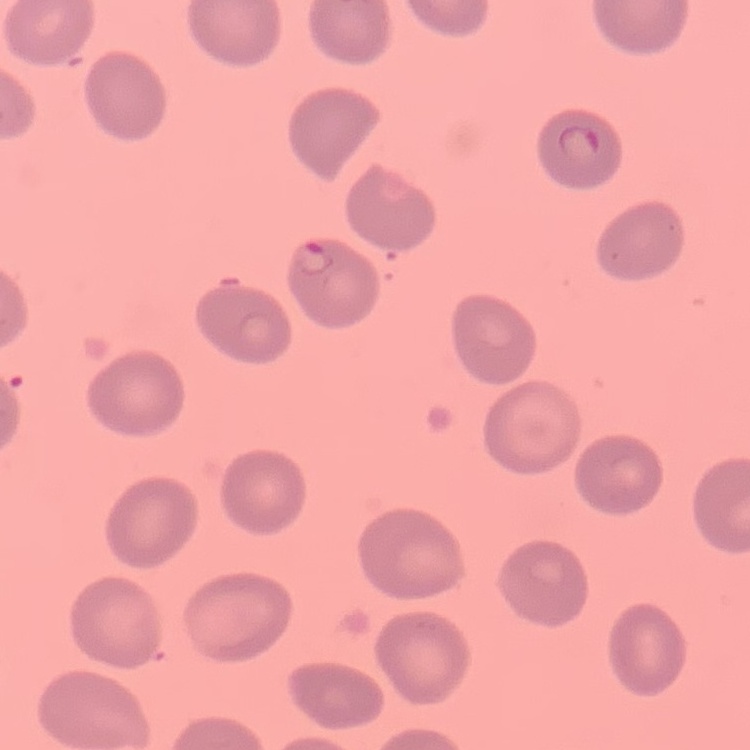

The red blood cells exhibit no rouleaux formation. Thin blood film. Stained with either Field's or Giemsa. Square crop of a larger photomicrograph.